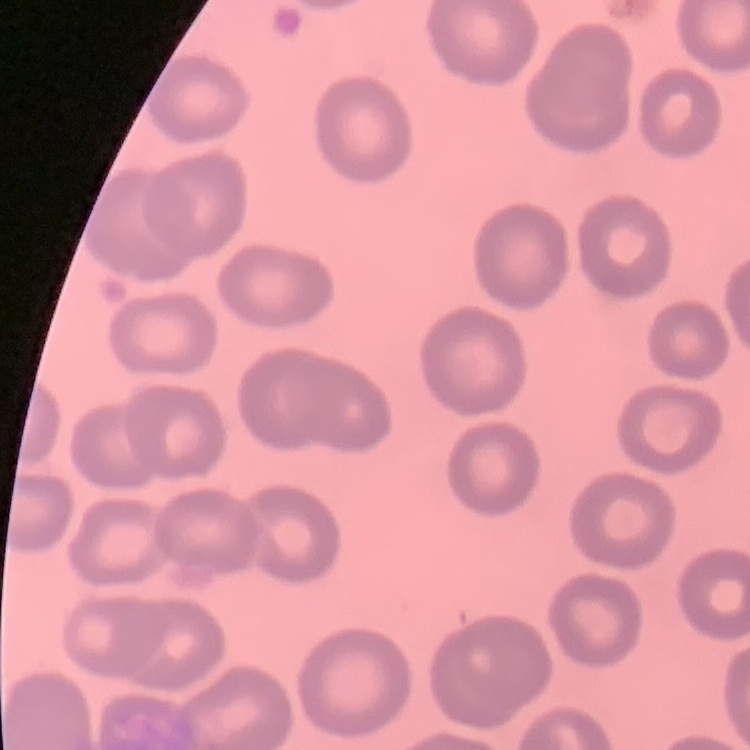 The red blood cells show no rouleaux formation. Square crop of a larger photomicrograph. Stained with either Field's or Giemsa. Thin peripheral smear.